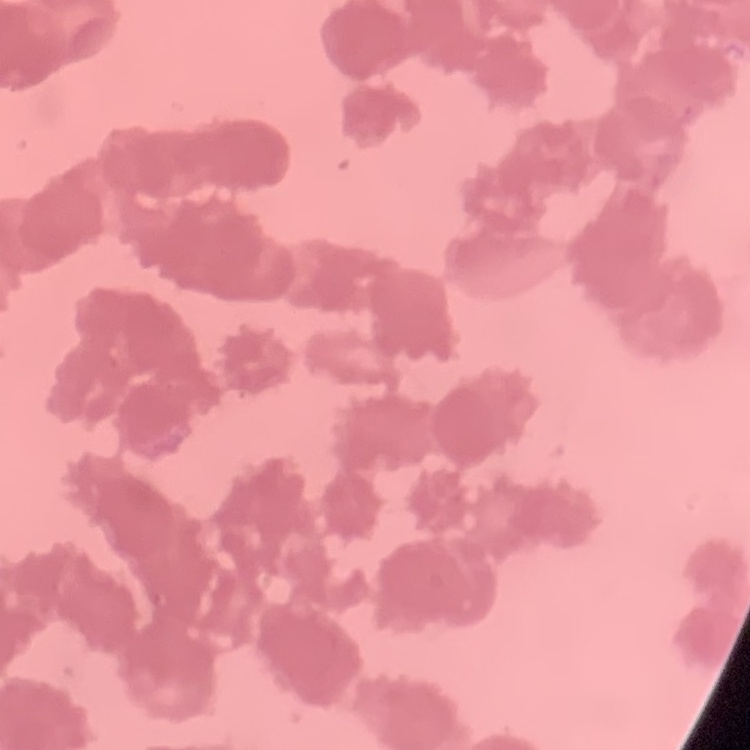
Summary:
  - Erythrocyte morphology: rouleaux formation
  - Image type: one tile cut from a larger photomicrograph
  - Stain: Field's or Giemsa
  - Preparation: thin blood film